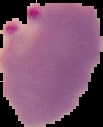

Image is 103×127 pixels. Cell region segmented out of the field of view; the surrounding area is masked to black. From a thin blood film. Result: Plasmodium parasites identified.